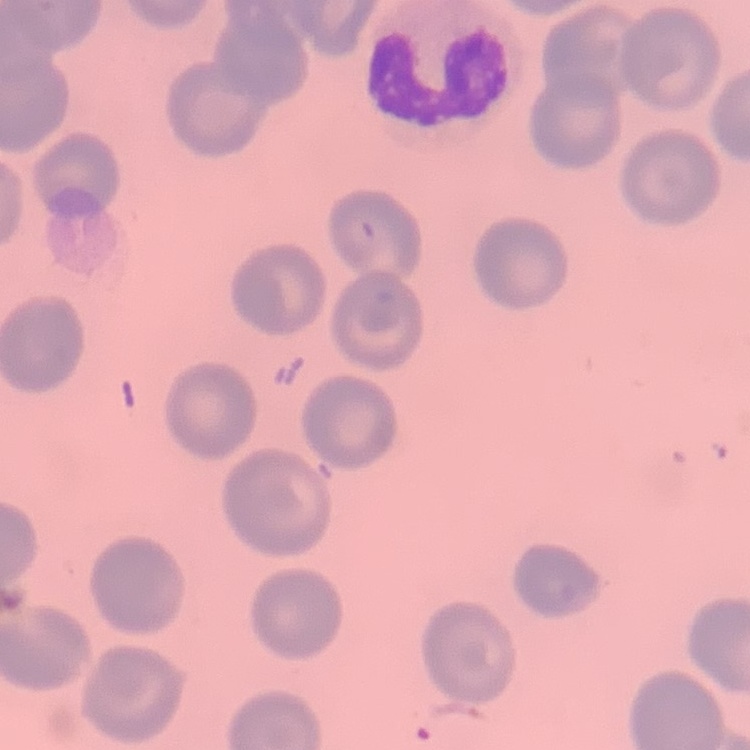
The red blood cells show no rouleaux formation. One tile cut from a larger photomicrograph. Stained with either Field's or Giemsa. Thin peripheral smear.